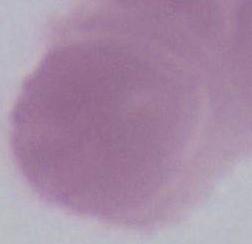

A red blood cell is seen. 1000x magnification. Photomicrograph.